Mark where platelets are.
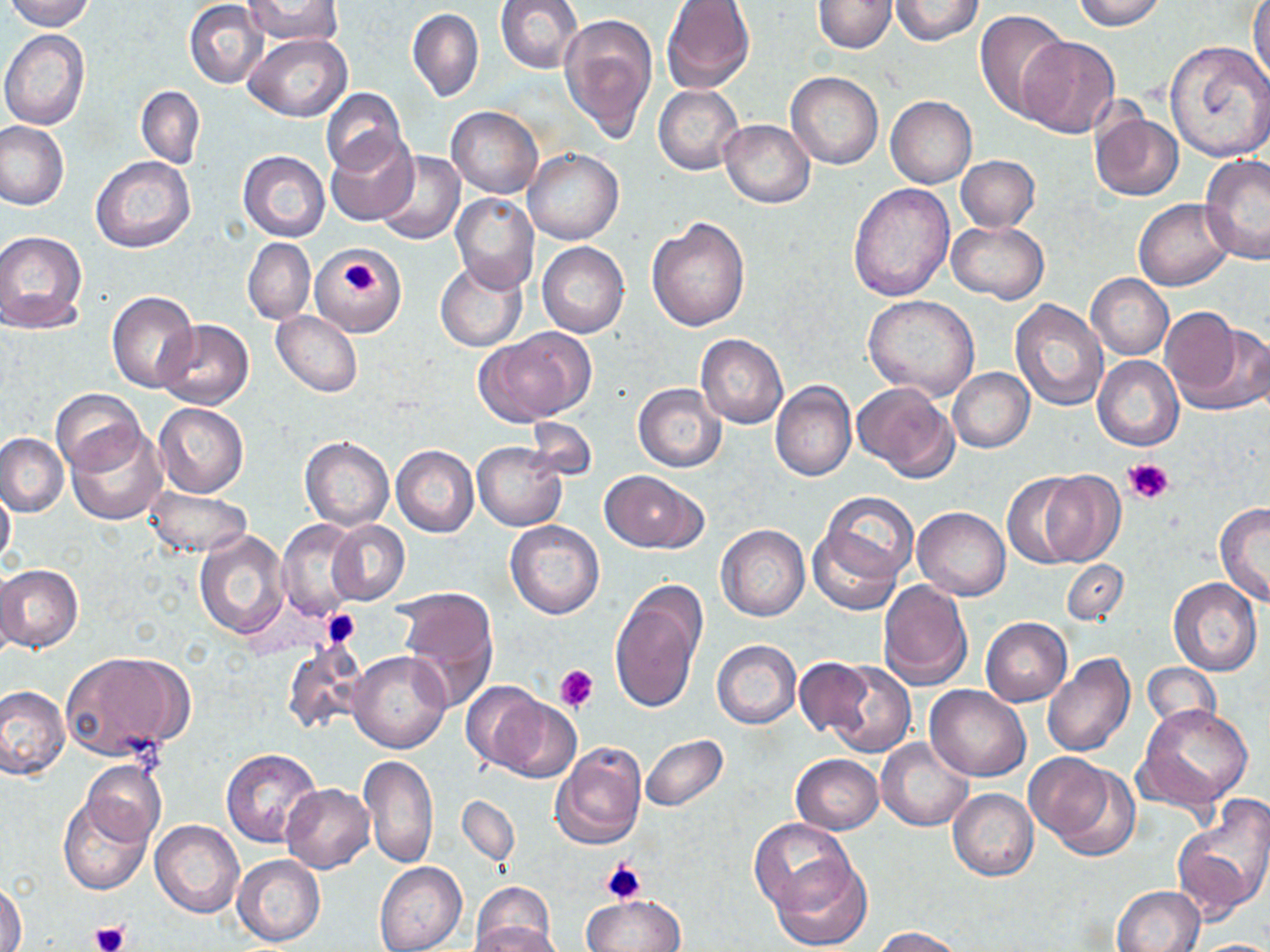

Approximate bounding boxes as named x1/y1/x2/y2 corners in pixels.
Platelets: (x1=343, y1=260, x2=378, y2=289), (x1=1123, y1=457, x2=1175, y2=505), (x1=321, y1=609, x2=362, y2=649), (x1=554, y1=664, x2=598, y2=713), (x1=599, y1=860, x2=648, y2=904), (x1=90, y1=920, x2=128, y2=951).

slide-level diagnosis = no evidence of blood parasites
field of view = one of a larger specimen
modality = light microscopy
uninfected red blood cell locations = approximate bounding boxes as named x1/y1/x2/y2 corners in pixels: (x1=6, y1=0, x2=95, y2=31), (x1=241, y1=0, x2=343, y2=48), (x1=495, y1=0, x2=583, y2=74), (x1=813, y1=0, x2=895, y2=53), (x1=890, y1=0, x2=983, y2=46), (x1=1070, y1=0, x2=1167, y2=31), (x1=661, y1=1, x2=754, y2=95), (x1=185, y1=2, x2=269, y2=87), (x1=1250, y1=2, x2=1270, y2=87), (x1=408, y1=8, x2=483, y2=102), (x1=974, y1=10, x2=1074, y2=120), (x1=560, y1=13, x2=658, y2=143), (x1=0, y1=30, x2=89, y2=129), (x1=244, y1=32, x2=351, y2=121), (x1=1018, y1=36, x2=1120, y2=139), (x1=1165, y1=41, x2=1270, y2=161), (x1=786, y1=71, x2=883, y2=169), (x1=654, y1=84, x2=744, y2=176), (x1=136, y1=85, x2=205, y2=168), (x1=322, y1=87, x2=406, y2=175), (x1=886, y1=96, x2=976, y2=188), (x1=447, y1=106, x2=543, y2=199), (x1=1090, y1=111, x2=1184, y2=201), (x1=719, y1=119, x2=815, y2=208), (x1=0, y1=121, x2=70, y2=210), (x1=326, y1=130, x2=419, y2=225), (x1=523, y1=148, x2=623, y2=245), (x1=238, y1=150, x2=329, y2=242), (x1=374, y1=151, x2=464, y2=245), (x1=91, y1=155, x2=195, y2=253), (x1=956, y1=155, x2=1039, y2=232), (x1=1200, y1=155, x2=1270, y2=264), (x1=846, y1=182, x2=953, y2=304), (x1=451, y1=192, x2=539, y2=292), (x1=1134, y1=198, x2=1235, y2=290), (x1=647, y1=215, x2=750, y2=333), (x1=946, y1=220, x2=1049, y2=303), (x1=0, y1=231, x2=89, y2=332), (x1=243, y1=237, x2=315, y2=325), (x1=537, y1=242, x2=629, y2=339), (x1=312, y1=245, x2=409, y2=341), (x1=434, y1=260, x2=527, y2=352), (x1=1087, y1=275, x2=1173, y2=359), (x1=106, y1=291, x2=198, y2=393), (x1=863, y1=294, x2=980, y2=398), (x1=1009, y1=298, x2=1108, y2=410), (x1=272, y1=310, x2=362, y2=397), (x1=1163, y1=311, x2=1268, y2=414), (x1=157, y1=320, x2=254, y2=410), (x1=477, y1=328, x2=593, y2=426), (x1=695, y1=334, x2=788, y2=429), (x1=1093, y1=356, x2=1184, y2=451), (x1=947, y1=368, x2=1034, y2=452), (x1=771, y1=382, x2=856, y2=483), (x1=854, y1=382, x2=959, y2=481), (x1=633, y1=384, x2=725, y2=472), (x1=52, y1=390, x2=145, y2=474), (x1=153, y1=401, x2=249, y2=498), (x1=524, y1=417, x2=598, y2=481), (x1=67, y1=425, x2=167, y2=525), (x1=0, y1=432, x2=68, y2=517), (x1=299, y1=436, x2=393, y2=531), (x1=472, y1=440, x2=566, y2=531), (x1=391, y1=445, x2=478, y2=538), (x1=601, y1=470, x2=705, y2=551), (x1=1035, y1=472, x2=1126, y2=566), (x1=1002, y1=473, x2=1092, y2=569), (x1=1, y1=480, x2=16, y2=573), (x1=144, y1=486, x2=251, y2=558), (x1=813, y1=490, x2=919, y2=588), (x1=1214, y1=503, x2=1270, y2=606), (x1=913, y1=507, x2=1009, y2=600), (x1=276, y1=520, x2=366, y2=619), (x1=327, y1=520, x2=409, y2=607), (x1=505, y1=520, x2=605, y2=619), (x1=716, y1=524, x2=809, y2=622), (x1=807, y1=524, x2=906, y2=616), (x1=193, y1=530, x2=291, y2=638), (x1=1060, y1=559, x2=1129, y2=625), (x1=0, y1=564, x2=84, y2=654), (x1=0, y1=565, x2=25, y2=663), (x1=1168, y1=578, x2=1262, y2=675), (x1=610, y1=579, x2=707, y2=715), (x1=877, y1=579, x2=973, y2=691), (x1=395, y1=589, x2=499, y2=707), (x1=981, y1=618, x2=1072, y2=706), (x1=281, y1=639, x2=369, y2=735), (x1=712, y1=640, x2=802, y2=728), (x1=347, y1=650, x2=453, y2=754), (x1=60, y1=651, x2=194, y2=760), (x1=1041, y1=654, x2=1135, y2=757), (x1=793, y1=658, x2=873, y2=737), (x1=821, y1=659, x2=915, y2=757), (x1=1142, y1=663, x2=1219, y2=732), (x1=460, y1=681, x2=548, y2=773), (x1=0, y1=684, x2=69, y2=781), (x1=926, y1=686, x2=1031, y2=782), (x1=486, y1=696, x2=582, y2=783), (x1=1138, y1=704, x2=1253, y2=810), (x1=640, y1=735, x2=728, y2=812), (x1=877, y1=738, x2=973, y2=831), (x1=550, y1=742, x2=646, y2=852), (x1=221, y1=748, x2=323, y2=849), (x1=359, y1=754, x2=439, y2=868), (x1=790, y1=754, x2=883, y2=834), (x1=1027, y1=754, x2=1139, y2=859), (x1=81, y1=759, x2=166, y2=848), (x1=281, y1=784, x2=375, y2=873), (x1=948, y1=788, x2=1039, y2=881), (x1=1173, y1=794, x2=1270, y2=920), (x1=57, y1=795, x2=153, y2=896), (x1=457, y1=796, x2=520, y2=867), (x1=749, y1=818, x2=852, y2=914), (x1=150, y1=819, x2=244, y2=917), (x1=232, y1=854, x2=327, y2=947), (x1=771, y1=854, x2=873, y2=950), (x1=375, y1=862, x2=466, y2=952), (x1=0, y1=879, x2=25, y2=952), (x1=470, y1=883, x2=557, y2=952), (x1=1113, y1=885, x2=1205, y2=952), (x1=582, y1=895, x2=683, y2=952), (x1=469, y1=922, x2=566, y2=952), (x1=874, y1=927, x2=966, y2=951), (x1=1193, y1=938, x2=1270, y2=951)
image size = 1270×952 pixels
magnification = 1000x
preparation = thin blood film
stain = May-Grünwald-Giemsa